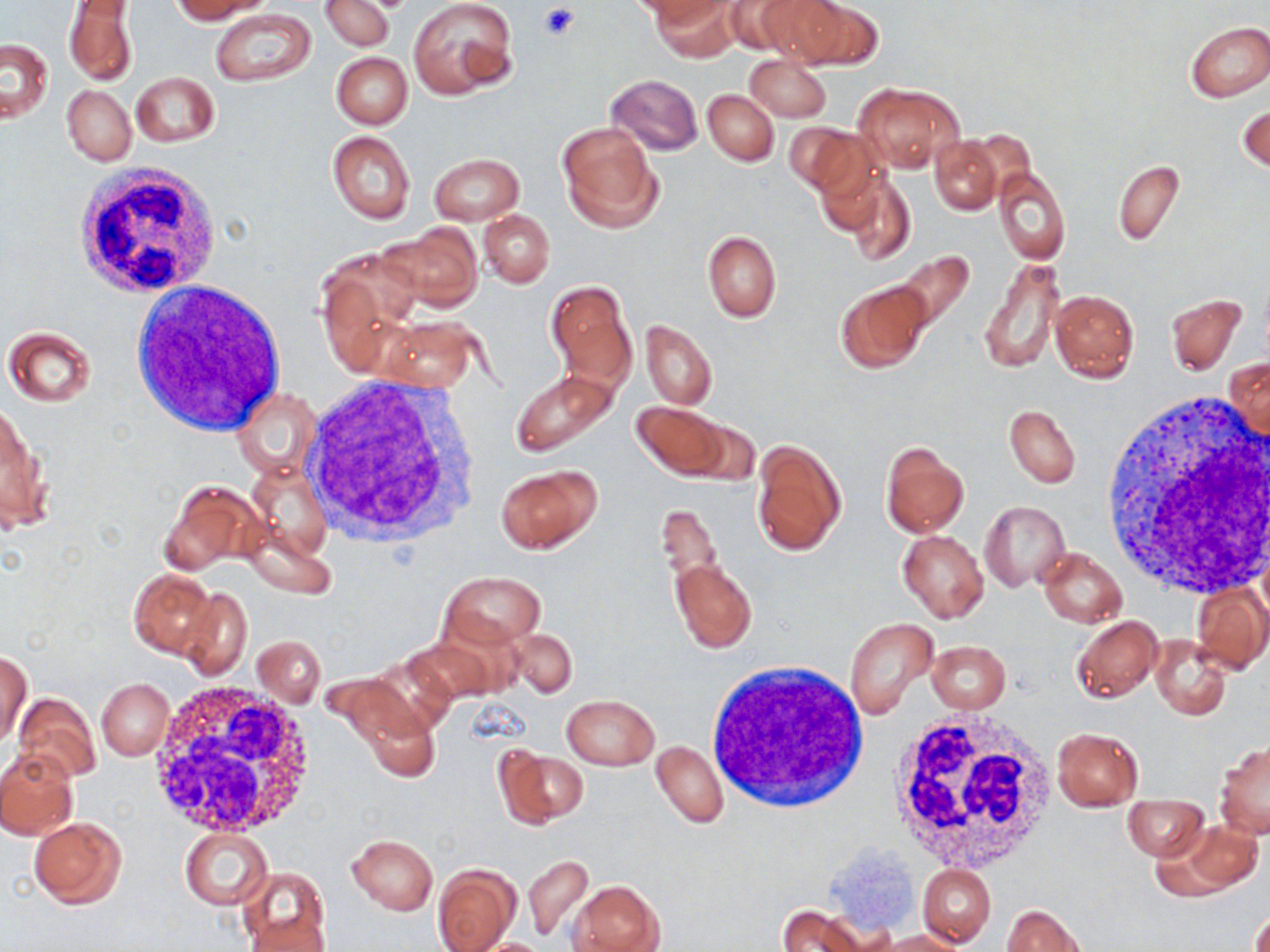 Approximate bounding boxes as named x1/y1/x2/y2 corners in pixels. Platelet locations: (x1=540, y1=4, x2=580, y2=41). Uninfected red blood cell locations: (x1=168, y1=0, x2=266, y2=23), (x1=408, y1=0, x2=518, y2=99), (x1=650, y1=0, x2=737, y2=61), (x1=723, y1=0, x2=827, y2=57), (x1=774, y1=0, x2=883, y2=68), (x1=320, y1=1, x2=394, y2=52), (x1=63, y1=2, x2=137, y2=88), (x1=210, y1=8, x2=316, y2=87), (x1=1184, y1=21, x2=1270, y2=103), (x1=2, y1=37, x2=53, y2=123), (x1=331, y1=51, x2=412, y2=129), (x1=745, y1=54, x2=831, y2=121), (x1=131, y1=71, x2=220, y2=147), (x1=605, y1=73, x2=702, y2=155), (x1=854, y1=82, x2=963, y2=171), (x1=62, y1=86, x2=136, y2=165), (x1=702, y1=89, x2=778, y2=165), (x1=1238, y1=103, x2=1269, y2=173), (x1=557, y1=123, x2=661, y2=230), (x1=786, y1=123, x2=875, y2=197), (x1=327, y1=131, x2=415, y2=225), (x1=929, y1=137, x2=1001, y2=214), (x1=429, y1=153, x2=524, y2=224), (x1=1113, y1=159, x2=1184, y2=246), (x1=992, y1=167, x2=1070, y2=264), (x1=842, y1=176, x2=916, y2=266), (x1=478, y1=210, x2=554, y2=287), (x1=382, y1=221, x2=482, y2=311), (x1=702, y1=230, x2=782, y2=323), (x1=888, y1=250, x2=977, y2=338), (x1=980, y1=256, x2=1065, y2=374), (x1=545, y1=280, x2=636, y2=390), (x1=835, y1=280, x2=932, y2=372), (x1=1049, y1=289, x2=1139, y2=382), (x1=1166, y1=293, x2=1247, y2=375), (x1=379, y1=317, x2=480, y2=391), (x1=641, y1=321, x2=716, y2=410), (x1=3, y1=327, x2=97, y2=407), (x1=1227, y1=359, x2=1269, y2=441), (x1=509, y1=369, x2=620, y2=457), (x1=232, y1=387, x2=319, y2=480), (x1=633, y1=401, x2=728, y2=478), (x1=1, y1=404, x2=47, y2=531), (x1=1004, y1=405, x2=1080, y2=488), (x1=673, y1=417, x2=760, y2=487), (x1=752, y1=439, x2=847, y2=556), (x1=880, y1=441, x2=968, y2=538), (x1=245, y1=465, x2=332, y2=562), (x1=496, y1=466, x2=598, y2=553), (x1=162, y1=480, x2=259, y2=576), (x1=656, y1=497, x2=724, y2=612), (x1=980, y1=500, x2=1070, y2=590), (x1=236, y1=519, x2=337, y2=597), (x1=898, y1=529, x2=989, y2=624), (x1=1037, y1=547, x2=1127, y2=628), (x1=670, y1=557, x2=756, y2=652), (x1=129, y1=568, x2=218, y2=657), (x1=442, y1=570, x2=544, y2=647), (x1=1190, y1=582, x2=1269, y2=675), (x1=178, y1=587, x2=253, y2=679), (x1=1071, y1=615, x2=1162, y2=702), (x1=842, y1=617, x2=936, y2=719), (x1=417, y1=621, x2=521, y2=699), (x1=507, y1=629, x2=578, y2=698), (x1=1150, y1=633, x2=1233, y2=721), (x1=253, y1=635, x2=325, y2=707), (x1=926, y1=640, x2=1011, y2=713), (x1=1, y1=653, x2=31, y2=747), (x1=97, y1=679, x2=173, y2=760), (x1=13, y1=692, x2=101, y2=783), (x1=561, y1=693, x2=660, y2=770), (x1=354, y1=695, x2=440, y2=781), (x1=1051, y1=727, x2=1143, y2=810), (x1=650, y1=739, x2=729, y2=829), (x1=1216, y1=740, x2=1270, y2=839), (x1=494, y1=747, x2=587, y2=829), (x1=0, y1=750, x2=77, y2=841), (x1=1123, y1=794, x2=1208, y2=859), (x1=27, y1=817, x2=127, y2=908), (x1=1174, y1=819, x2=1265, y2=895), (x1=180, y1=828, x2=273, y2=910), (x1=345, y1=834, x2=438, y2=915), (x1=523, y1=854, x2=593, y2=942), (x1=433, y1=864, x2=520, y2=951), (x1=917, y1=864, x2=996, y2=947), (x1=237, y1=868, x2=329, y2=950), (x1=569, y1=880, x2=661, y2=952), (x1=1249, y1=900, x2=1270, y2=952), (x1=774, y1=905, x2=869, y2=952), (x1=1001, y1=905, x2=1086, y2=951), (x1=247, y1=913, x2=331, y2=952), (x1=877, y1=930, x2=962, y2=951), (x1=466, y1=938, x2=554, y2=952). White blood cell locations: (x1=72, y1=162, x2=223, y2=302), (x1=131, y1=280, x2=286, y2=437), (x1=302, y1=374, x2=484, y2=548), (x1=294, y1=375, x2=484, y2=547), (x1=1097, y1=393, x2=1270, y2=600), (x1=704, y1=659, x2=872, y2=815), (x1=147, y1=682, x2=321, y2=838), (x1=889, y1=707, x2=1061, y2=872). Slide-level diagnosis: negative for blood parasites. Image is 1270×952 pixels. Thin blood film. May-Grünwald-Giemsa-stained preparation. One field of a larger specimen. 1000x magnification. Optical microscopy.